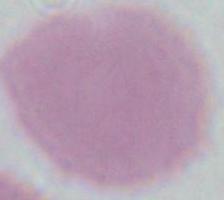
modality = micrograph
magnification = 1000x
identification = red blood cell